State the blood parasite species.
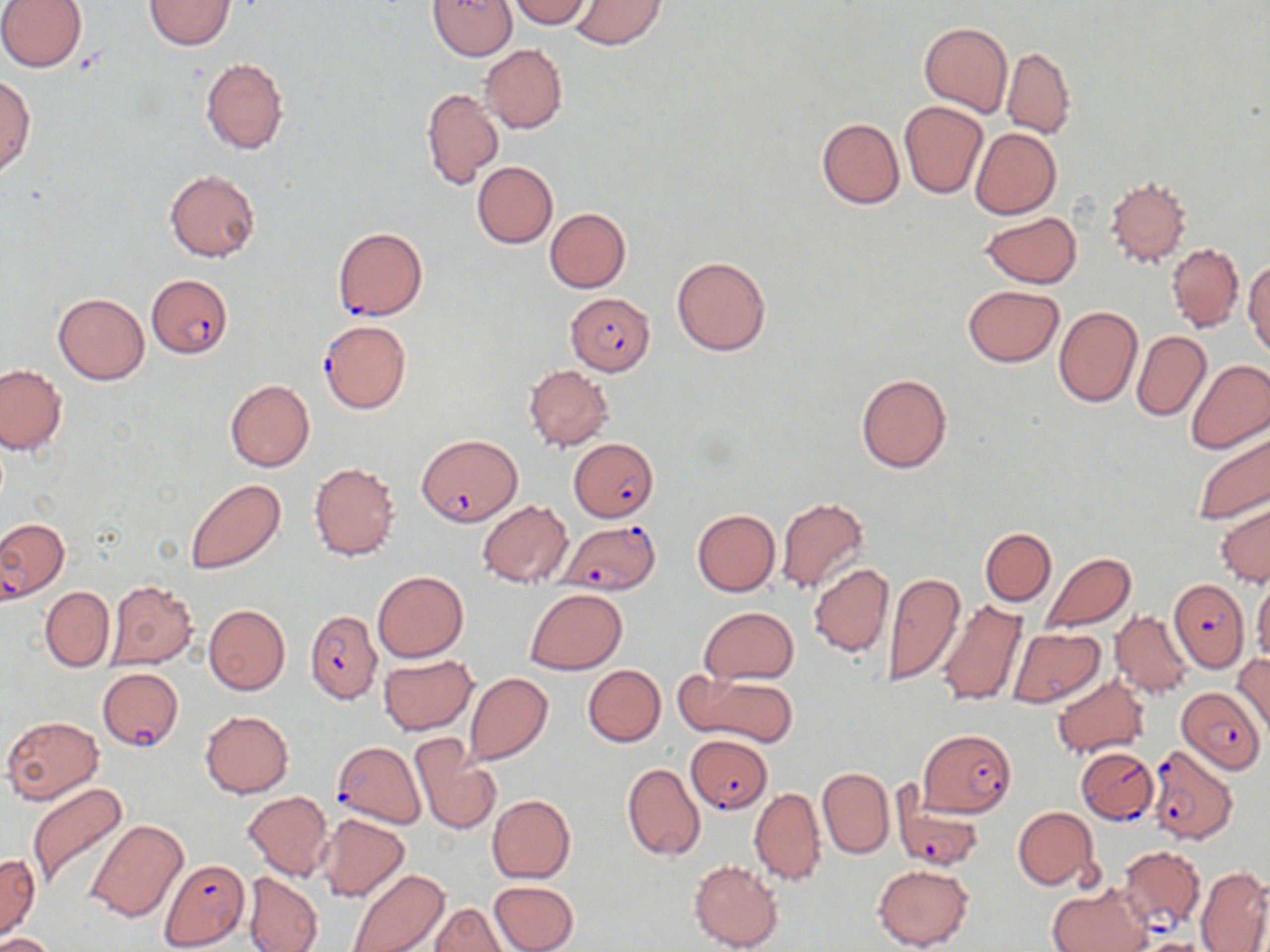
Plasmodium falciparum.

Summary:
  - Coordinate format: approximate bounding boxes as [x1, y1, x2, y2] in pixels
  - Plasmodium falciparum-infected red blood cell locations: [332, 227, 427, 320], [146, 274, 233, 358], [565, 293, 656, 375], [319, 320, 411, 414], [416, 433, 522, 526], [569, 438, 659, 522], [0, 516, 69, 601], [559, 519, 659, 596], [1167, 579, 1248, 671], [306, 608, 381, 704], [97, 666, 184, 753], [1177, 688, 1265, 772], [917, 729, 1017, 815], [686, 735, 772, 814], [331, 740, 425, 829], [1155, 744, 1238, 846], [1077, 747, 1159, 824], [891, 791, 987, 874], [1118, 845, 1205, 932], [161, 859, 249, 949]
  - Uninfected red blood cell locations: [0, 0, 87, 71], [145, 0, 235, 49], [427, 0, 517, 59], [508, 0, 590, 27], [568, 0, 667, 51], [919, 21, 1011, 118], [480, 45, 568, 134], [1001, 48, 1075, 138], [200, 57, 288, 154], [0, 74, 34, 176], [421, 87, 503, 190], [899, 100, 987, 198], [816, 117, 904, 209], [970, 128, 1061, 219], [471, 161, 557, 248], [163, 169, 260, 263], [1104, 177, 1193, 268], [545, 208, 631, 293], [980, 211, 1081, 288], [1166, 243, 1243, 332], [672, 255, 772, 356], [1244, 260, 1270, 357], [962, 285, 1065, 367], [54, 292, 149, 385], [1053, 305, 1143, 407], [1131, 331, 1210, 422], [1186, 359, 1270, 454], [524, 364, 613, 451], [0, 365, 66, 454], [855, 372, 952, 474], [225, 379, 315, 472], [1189, 428, 1270, 526], [309, 463, 400, 562], [185, 478, 286, 575], [775, 497, 870, 597], [477, 499, 572, 586], [1216, 501, 1270, 587], [692, 508, 780, 596], [980, 528, 1056, 605], [1040, 552, 1137, 634], [808, 563, 895, 658], [372, 571, 468, 661], [882, 571, 964, 689], [106, 580, 198, 669], [1253, 580, 1270, 661], [42, 586, 114, 672], [525, 589, 625, 674], [936, 601, 1028, 706], [203, 604, 290, 695], [699, 607, 798, 683], [1110, 610, 1195, 698], [1006, 627, 1105, 707], [378, 656, 477, 734], [1233, 656, 1270, 737], [582, 664, 665, 747], [691, 672, 796, 747], [465, 673, 553, 764], [1050, 674, 1150, 759], [200, 711, 293, 798], [2, 715, 104, 804], [409, 736, 501, 837], [622, 763, 705, 861], [818, 767, 893, 859], [26, 782, 129, 894], [749, 786, 826, 885], [243, 791, 333, 881], [487, 794, 575, 883], [1011, 806, 1099, 890], [316, 814, 410, 901], [84, 817, 189, 922], [0, 854, 41, 939], [688, 860, 783, 952], [872, 864, 972, 950], [1195, 866, 1270, 952], [347, 867, 449, 952], [243, 872, 323, 951], [489, 880, 578, 951], [1047, 885, 1151, 952], [430, 903, 506, 951], [1, 931, 57, 952], [1132, 938, 1217, 952]
  - Field of view: one of a larger specimen
  - Magnification: 1000x
  - Modality: optical microscopy
  - Image size: 1270×952 pixels
  - Preparation: thin blood film
  - Stain: May-Grünwald-Giemsa